State which parasite is depicted.
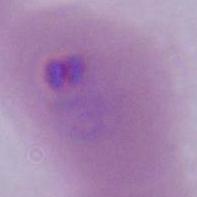

Plasmodium.

Micrograph. 400x or 1000x magnification.